Assess this cell for malaria.
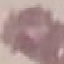

It is uninfected.

Giemsa-stained preparation. Thin blood film. Cell patch, automatically extracted from a larger field of view and resized to 64 × 64 pixels. Acquired by smartphone through the microscope eyepiece.